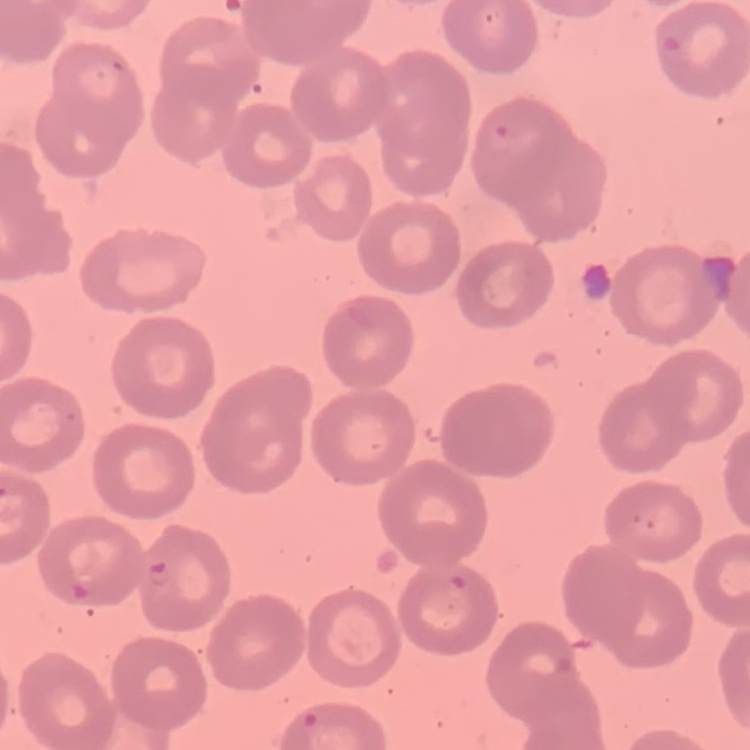

The erythrocytes exhibit no rouleaux formation. Thin peripheral smear. Square crop of a larger photomicrograph. Field's or Giemsa stain.